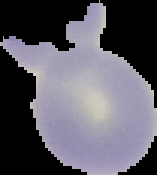

Result: no Plasmodium parasites seen. Image is 157×175 pixels. From a thin blood smear. Cell region segmented out of the field of view; the surrounding area is masked to black.